Classify this cell by malaria status.
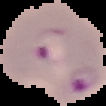
Parasitized.

image_type: segmented cell region with the area outside set to black
preparation: thin blood smear
image_size: 106×106 pixels